Identify the blood parasite species.
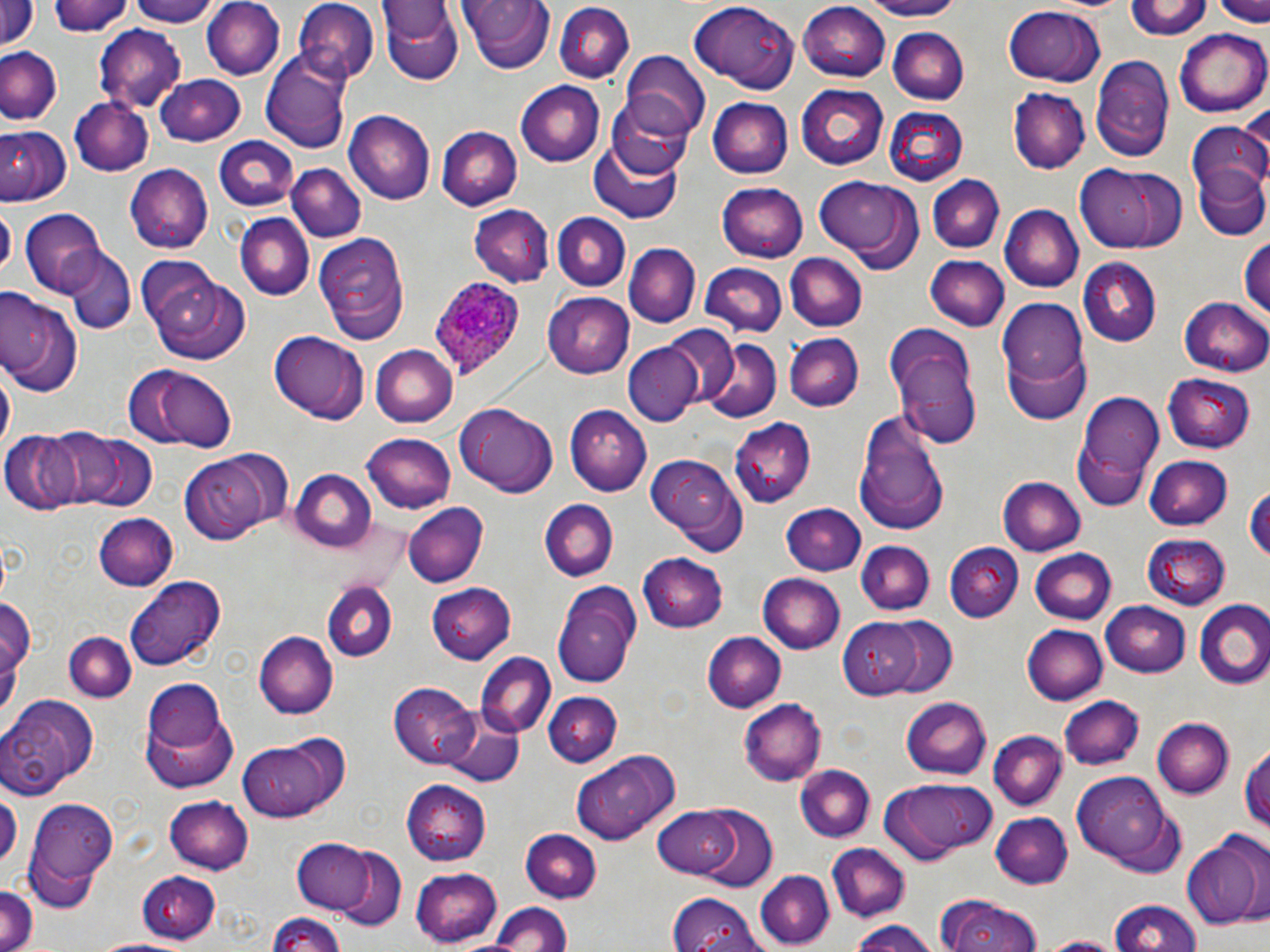

Plasmodium ovale.

Summary:
  - Coordinate format: approximate bounding boxes as (x1,y1)-(x2,y2) corner pairs in pixels
  - Plasmodium ovale-infected red blood cell locations: (429,273)-(526,381)
  - Uninfected red blood cell locations: (46,0)-(131,36), (125,0)-(219,25), (202,0)-(285,80), (459,0)-(555,73), (851,0)-(972,21), (1128,0)-(1212,41), (1214,0)-(1270,26), (0,1)-(38,54), (378,1)-(463,85), (296,3)-(380,87), (799,3)-(893,80), (553,4)-(636,84), (688,4)-(794,90), (1001,6)-(1106,86), (94,26)-(184,112), (888,27)-(969,104), (1177,27)-(1270,117), (0,47)-(61,126), (621,51)-(710,141), (262,52)-(354,153), (1091,53)-(1175,163), (154,75)-(247,145), (516,80)-(605,166), (796,85)-(890,170), (1009,88)-(1089,174), (606,91)-(698,177), (708,98)-(793,178), (70,99)-(154,176), (882,107)-(968,186), (344,111)-(435,204), (0,113)-(132,192), (1186,122)-(1270,215), (0,125)-(71,204), (436,126)-(521,211), (214,135)-(300,214), (590,136)-(689,225), (1076,163)-(1194,251), (1191,163)-(1270,243), (286,164)-(367,244), (124,165)-(212,254), (929,174)-(1004,253), (815,178)-(924,271), (715,183)-(807,262), (1,204)-(14,277), (469,205)-(555,288), (998,205)-(1083,293), (21,209)-(108,293), (553,212)-(631,289), (234,215)-(315,302), (313,233)-(409,344), (1241,237)-(1269,318), (624,243)-(699,325), (64,248)-(134,334), (785,252)-(867,332), (926,256)-(1008,331), (937,256)-(1061,351), (1077,259)-(1161,346), (701,263)-(786,336), (146,267)-(248,363), (0,292)-(82,397), (544,293)-(635,379), (1181,296)-(1270,375), (996,299)-(1088,386), (664,326)-(741,405), (885,328)-(983,449), (270,333)-(366,423), (785,333)-(864,412), (701,338)-(781,422), (372,343)-(460,428), (623,343)-(700,425), (1002,347)-(1092,425), (139,367)-(235,450), (1165,371)-(1256,451), (1073,391)-(1168,510), (456,403)-(559,496), (569,407)-(650,496), (853,412)-(949,533), (728,418)-(816,506), (49,428)-(145,514), (4,431)-(82,515), (360,433)-(455,513), (648,453)-(747,550), (180,454)-(275,544), (1145,456)-(1233,530), (292,469)-(378,551), (997,477)-(1087,555), (1244,486)-(1270,563), (538,498)-(618,582), (777,502)-(866,577), (405,504)-(487,587), (93,514)-(178,590), (1143,531)-(1231,608), (855,541)-(935,614), (946,543)-(1022,622), (1028,547)-(1116,622), (639,552)-(728,630), (757,573)-(845,654), (128,574)-(226,669), (425,582)-(516,665), (554,582)-(641,689), (323,584)-(395,662), (1191,599)-(1270,688), (1101,601)-(1193,678), (1020,615)-(1184,694), (881,616)-(956,696), (846,618)-(927,696), (1022,624)-(1108,706), (254,631)-(336,719), (65,632)-(137,701), (702,632)-(784,713), (476,653)-(555,738), (140,679)-(236,792), (390,684)-(481,766), (3,692)-(101,796), (543,693)-(621,767), (1058,695)-(1145,772), (899,696)-(991,779), (739,697)-(827,785), (442,713)-(525,786), (1153,718)-(1233,798), (988,731)-(1066,811), (236,737)-(341,822), (1242,741)-(1270,836), (574,752)-(677,843), (793,765)-(874,844), (1073,773)-(1171,860), (879,777)-(995,863), (404,779)-(492,864), (27,792)-(115,910), (166,797)-(255,872), (650,806)-(744,882), (693,808)-(778,893), (992,810)-(1074,888), (521,828)-(601,905), (1182,831)-(1268,928), (294,839)-(374,914), (826,844)-(908,921), (334,847)-(406,930), (409,866)-(501,946), (141,870)-(223,943), (755,870)-(835,948), (0,884)-(39,952), (668,893)-(764,951), (934,894)-(1044,952), (1107,899)-(1204,952), (487,901)-(572,952), (268,911)-(346,952), (848,919)-(940,952), (1035,935)-(1127,952)
  - Field of view: one of a larger specimen
  - Magnification: 1000x
  - Preparation: thin blood film
  - Image size: 1270×952 pixels
  - Modality: light microscopy
  - Stain: May-Grünwald-Giemsa